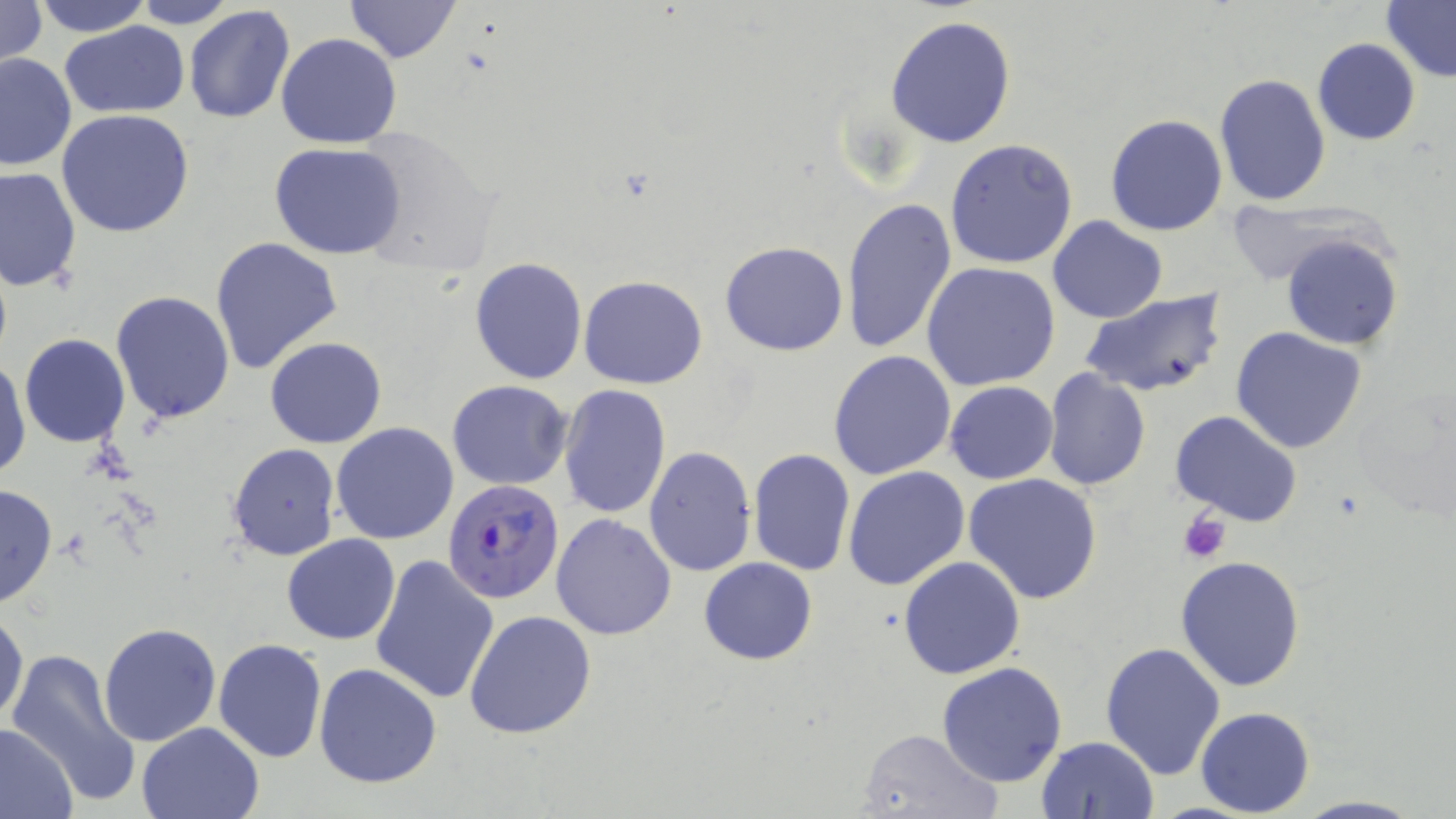
Summary:
  - Coordinate format: approximate bounding boxes as [x1, y1, x2, y2] in pixels
  - Uninfected red blood cell locations: [0, 0, 48, 73], [33, 0, 152, 37], [129, 0, 243, 28], [344, 0, 461, 63], [1381, 1, 1456, 85], [183, 5, 295, 126], [884, 14, 1017, 149], [59, 21, 191, 119], [275, 32, 403, 149], [1312, 38, 1421, 146], [0, 51, 76, 171], [1214, 73, 1330, 208], [57, 109, 195, 238], [1104, 114, 1228, 237], [347, 128, 500, 277], [945, 139, 1078, 268], [270, 143, 407, 260], [0, 167, 80, 293], [840, 198, 957, 356], [1223, 202, 1379, 286], [1046, 216, 1168, 323], [1281, 233, 1402, 351], [211, 236, 344, 375], [719, 241, 848, 357], [469, 257, 588, 385], [921, 261, 1061, 392], [579, 275, 707, 389], [1079, 289, 1228, 401], [112, 292, 236, 425], [1230, 328, 1367, 454], [18, 333, 131, 448], [264, 336, 388, 450], [828, 350, 958, 481], [1, 356, 30, 481], [1043, 369, 1150, 492], [447, 380, 574, 490], [944, 380, 1058, 484], [557, 384, 671, 520], [1348, 392, 1455, 516], [1171, 411, 1302, 529], [331, 423, 459, 546], [227, 443, 342, 563], [644, 447, 756, 576], [748, 447, 857, 578], [842, 466, 971, 591], [964, 475, 1103, 605], [0, 483, 57, 610], [550, 514, 677, 641], [281, 534, 401, 644], [369, 553, 501, 706], [898, 555, 1024, 678], [1175, 555, 1306, 693], [699, 557, 817, 664], [1, 607, 27, 729], [465, 608, 597, 739], [98, 624, 222, 746], [213, 639, 327, 762], [1098, 640, 1227, 779], [5, 648, 143, 807], [314, 662, 441, 788], [938, 662, 1069, 787], [1195, 707, 1316, 817], [137, 721, 265, 818], [0, 722, 79, 819], [855, 727, 1001, 817], [1036, 735, 1160, 819], [1293, 794, 1423, 818]
  - Platelet locations: [1177, 510, 1232, 563]
  - Plasmodium falciparum-infected red blood cell locations: [441, 479, 563, 604]
  - Slide-level diagnosis: Plasmodium falciparum
  - Stain: May-Grünwald-Giemsa
  - Field of view: single
  - Preparation: thin blood smear
  - Image size: 1456×819 pixels
  - Magnification: 1000x
  - Modality: optical microscopy